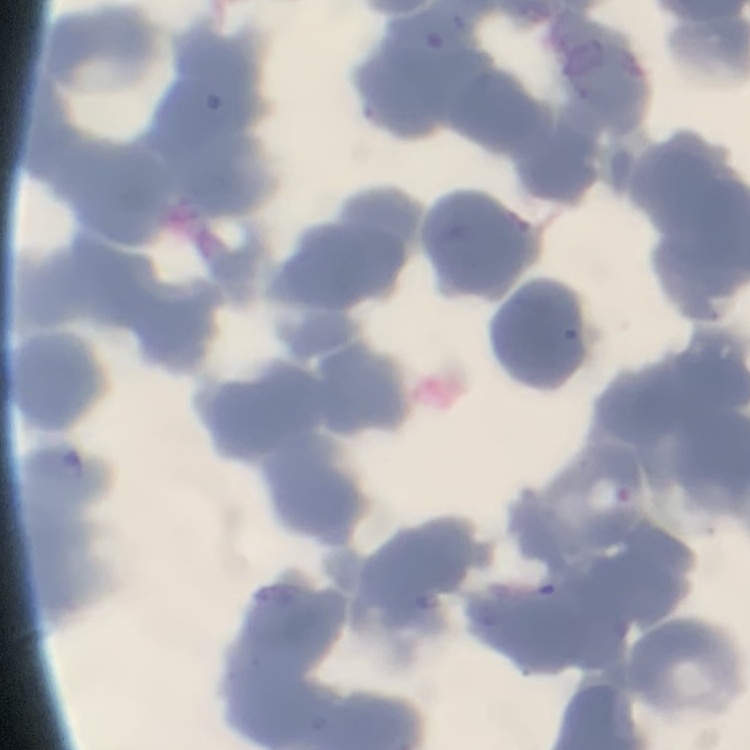

{
  "erythrocyte_morphology": "rouleaux formation",
  "stain": "Field's or Giemsa",
  "image_type": "one tile cut from a larger photomicrograph",
  "preparation": "thin blood film"
}